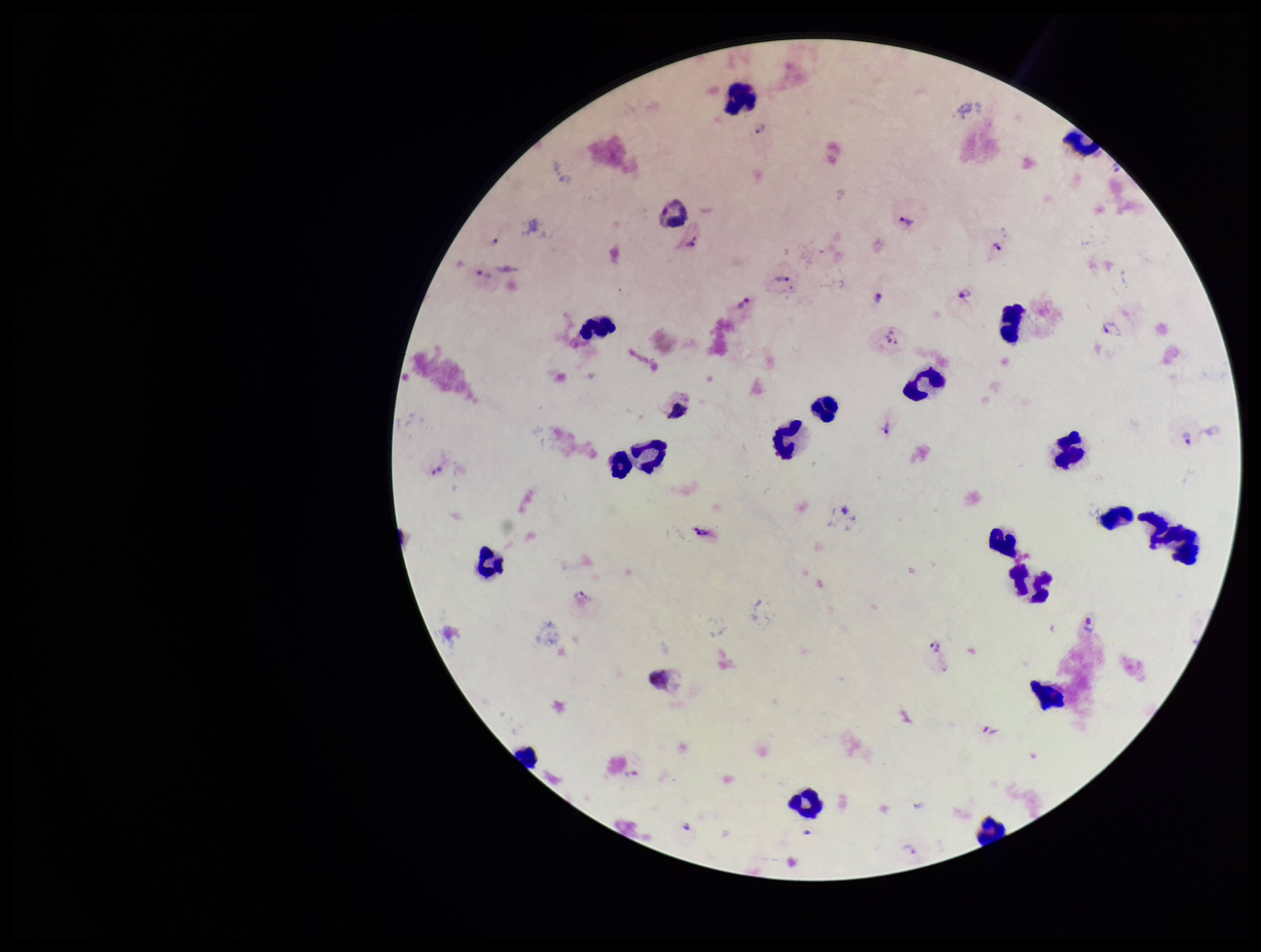

Summary:
  - Plasmodium parasites: seen
  - Capture: smartphone photograph through the microscope eyepiece
  - Patient malaria status: positive
  - Field of view: one from this slide
  - Parasite count: 24
  - Stain: Giemsa
  - Leukocyte count: 22
  - Image size: 1261×952 pixels
  - Preparation: thick smear
  - Species reported for this patient: Plasmodium vivax